Locate and identify every blood parasite.
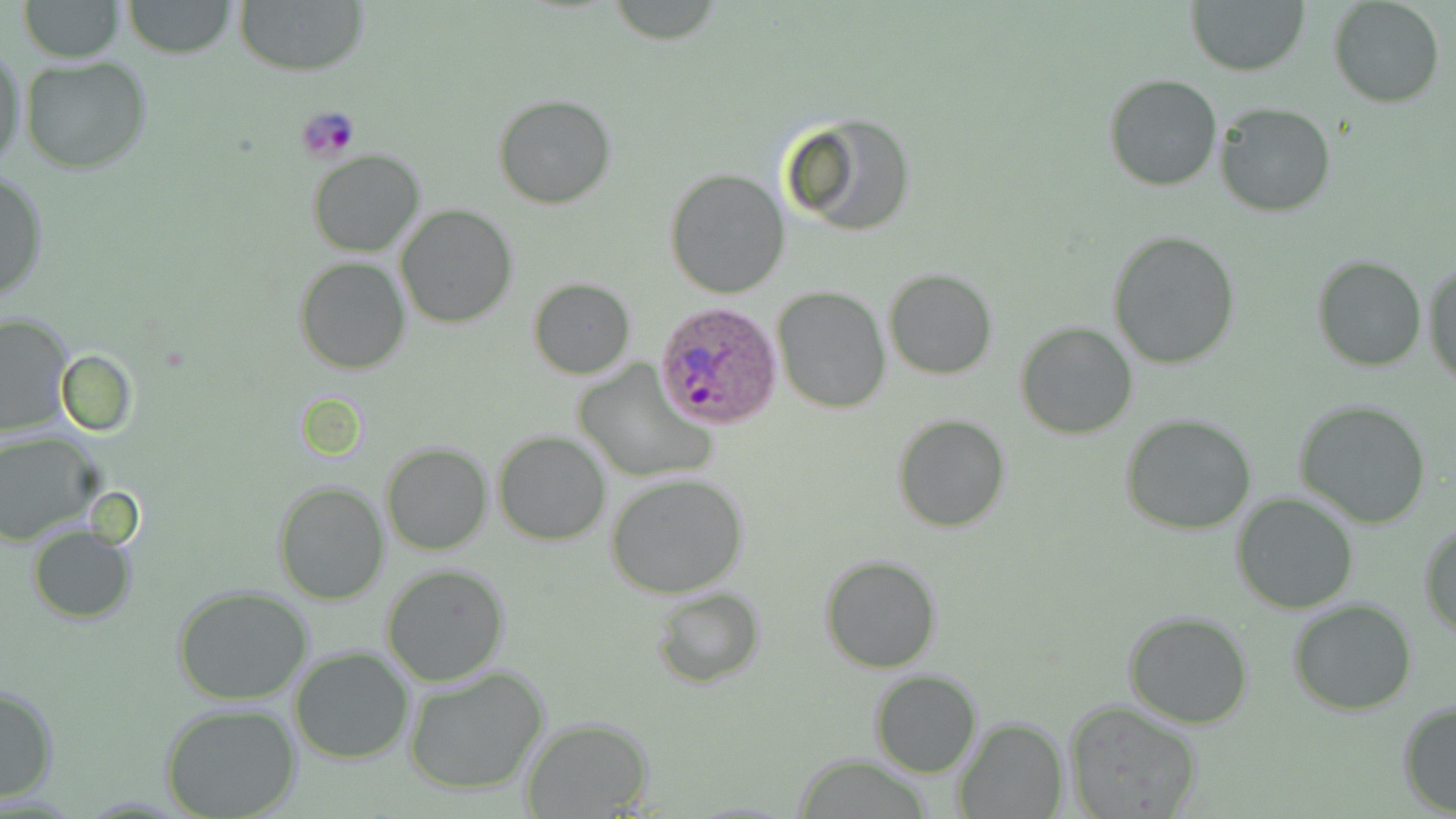

Approximate bounding boxes as (x1, y1, x2, y2) in pixels.
Plasmodium ovale-infected red blood cells: (655, 300, 782, 429).
No Plasmodium falciparum, Plasmodium malariae, Plasmodium vivax, Babesia divergens, or Trypanosoma brucei observed.

Platelet locations: (299, 106, 361, 162). Uninfected red blood cell locations: (17, 0, 125, 61), (121, 0, 238, 58), (234, 0, 367, 78), (1187, 0, 1309, 76), (1330, 0, 1444, 108), (0, 41, 27, 178), (18, 56, 154, 173), (1103, 74, 1221, 192), (493, 94, 618, 208), (1214, 101, 1336, 217), (780, 113, 918, 237), (307, 149, 425, 258), (664, 167, 789, 299), (1, 168, 47, 305), (395, 204, 517, 328), (1106, 231, 1242, 370), (1310, 254, 1429, 372), (1423, 256, 1456, 389), (295, 257, 410, 374), (884, 269, 997, 379), (528, 279, 635, 378), (773, 288, 890, 412), (0, 314, 73, 436), (1015, 321, 1140, 439), (574, 359, 715, 484), (1294, 398, 1433, 529), (1119, 414, 1258, 535), (894, 415, 1010, 532), (493, 430, 611, 545), (0, 432, 100, 545), (380, 442, 492, 555), (606, 472, 749, 597), (273, 480, 388, 604), (1231, 493, 1358, 614), (1418, 520, 1456, 636), (27, 527, 136, 623), (820, 554, 942, 673), (381, 561, 512, 685), (172, 586, 315, 707), (652, 587, 764, 689), (1289, 598, 1417, 714), (1123, 611, 1254, 730), (290, 646, 415, 765), (403, 664, 550, 796), (869, 671, 981, 777), (0, 685, 60, 802), (1061, 698, 1205, 819), (1397, 700, 1456, 816), (160, 702, 302, 819), (953, 717, 1069, 819), (519, 719, 655, 816), (790, 756, 941, 818). Slide-level diagnosis: Plasmodium ovale. Thin blood smear. Image is 1456×819 pixels. May-Grünwald-Giemsa stain. One field of a larger specimen. 1000x magnification. Light microscopy.